Assess the morphology of the red blood cells.
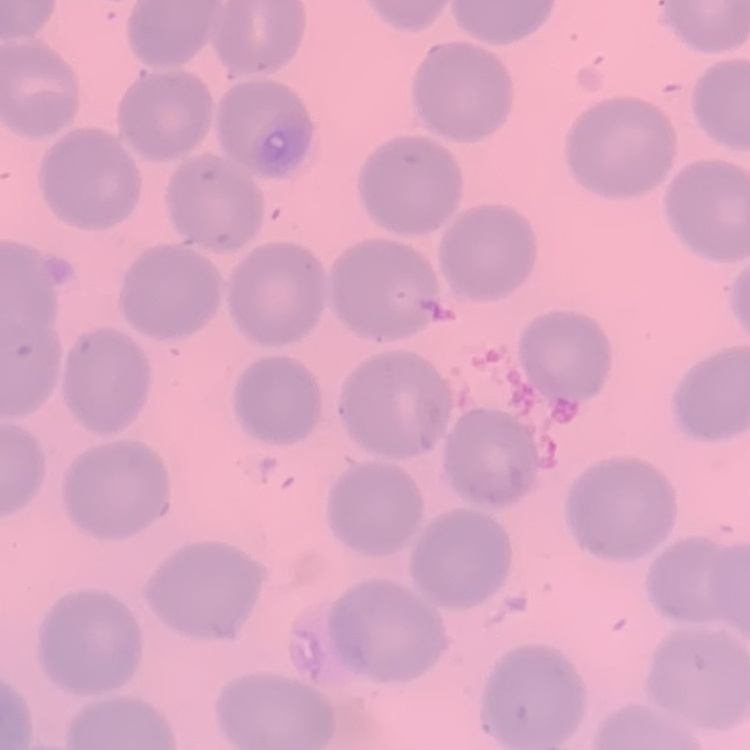

They show no rouleaux formation.

{
  "preparation": "thin blood film",
  "image_type": "square crop of a larger photomicrograph",
  "stain": "Field's or Giemsa"
}